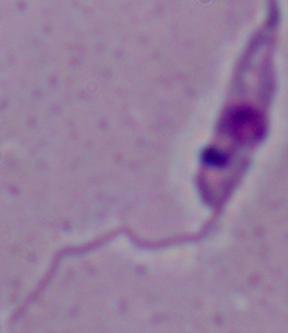

{
  "modality": "photomicrograph",
  "magnification": "1000x",
  "identification": "Leishmania"
}